Report the malaria status of this cell.
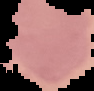

It is uninfected.

Cell region segmented out of the field of view; the surrounding area is masked to black. Image is 94×91 pixels. From a thin blood smear.